Comment on the morphology of the erythrocytes.
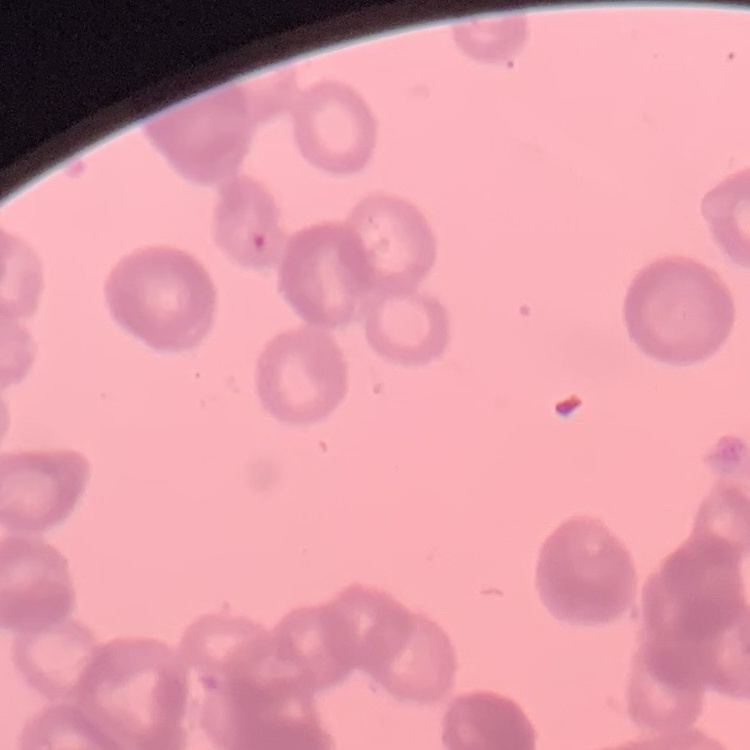

They show rouleaux formation.

preparation = thin blood film
stain = Field's or Giemsa
image type = square crop of a larger photomicrograph